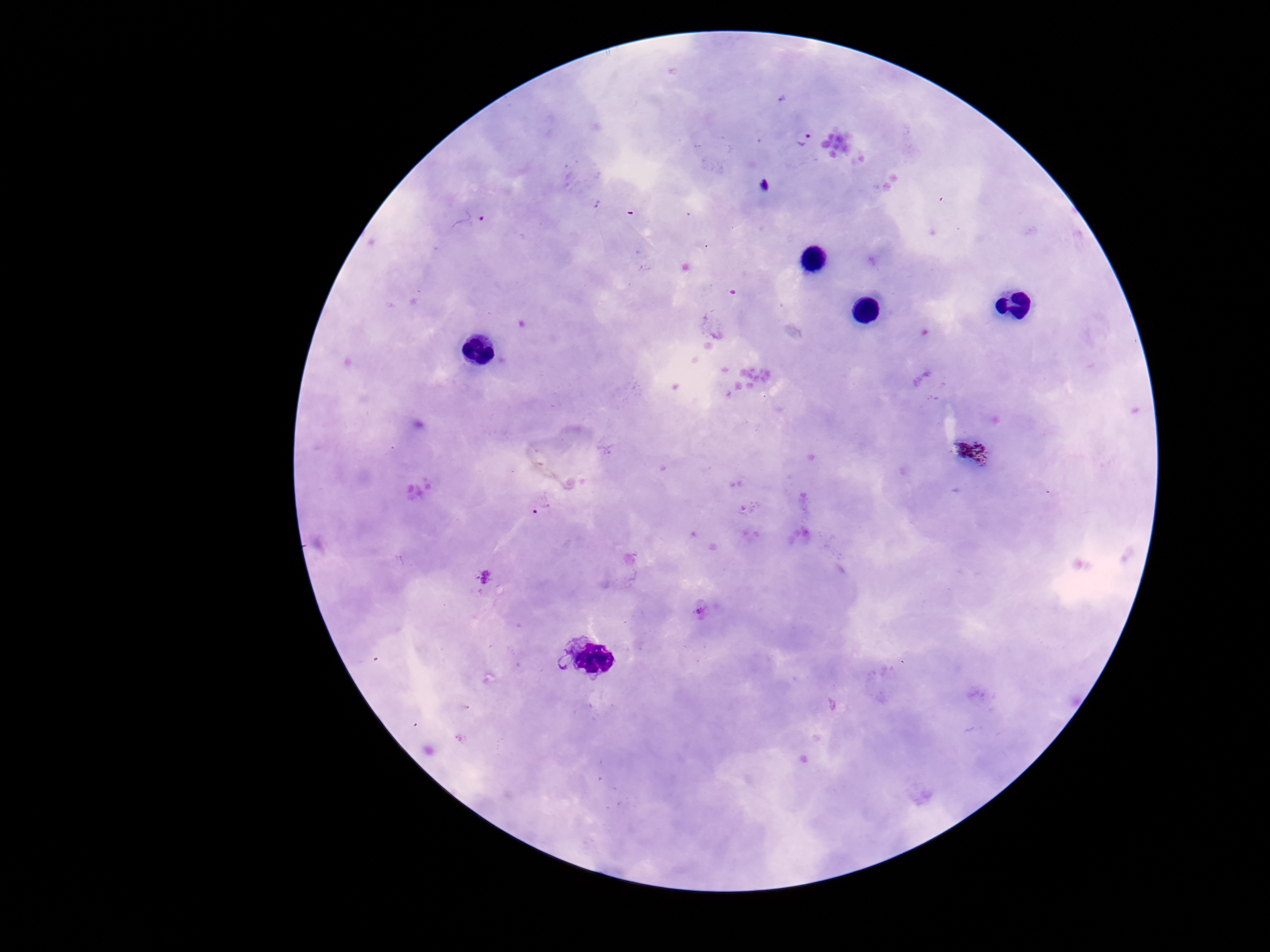
field of view = one from this slide
image size = 1270×952 pixels
stain = Giemsa
preparation = thick blood film
patient malaria status = infected
capture = smartphone camera through the microscope eyepiece
magnification = 100x
Plasmodium parasite locations = approximate centers as (x, y) in pixels: (804, 137)